Outline platelets.
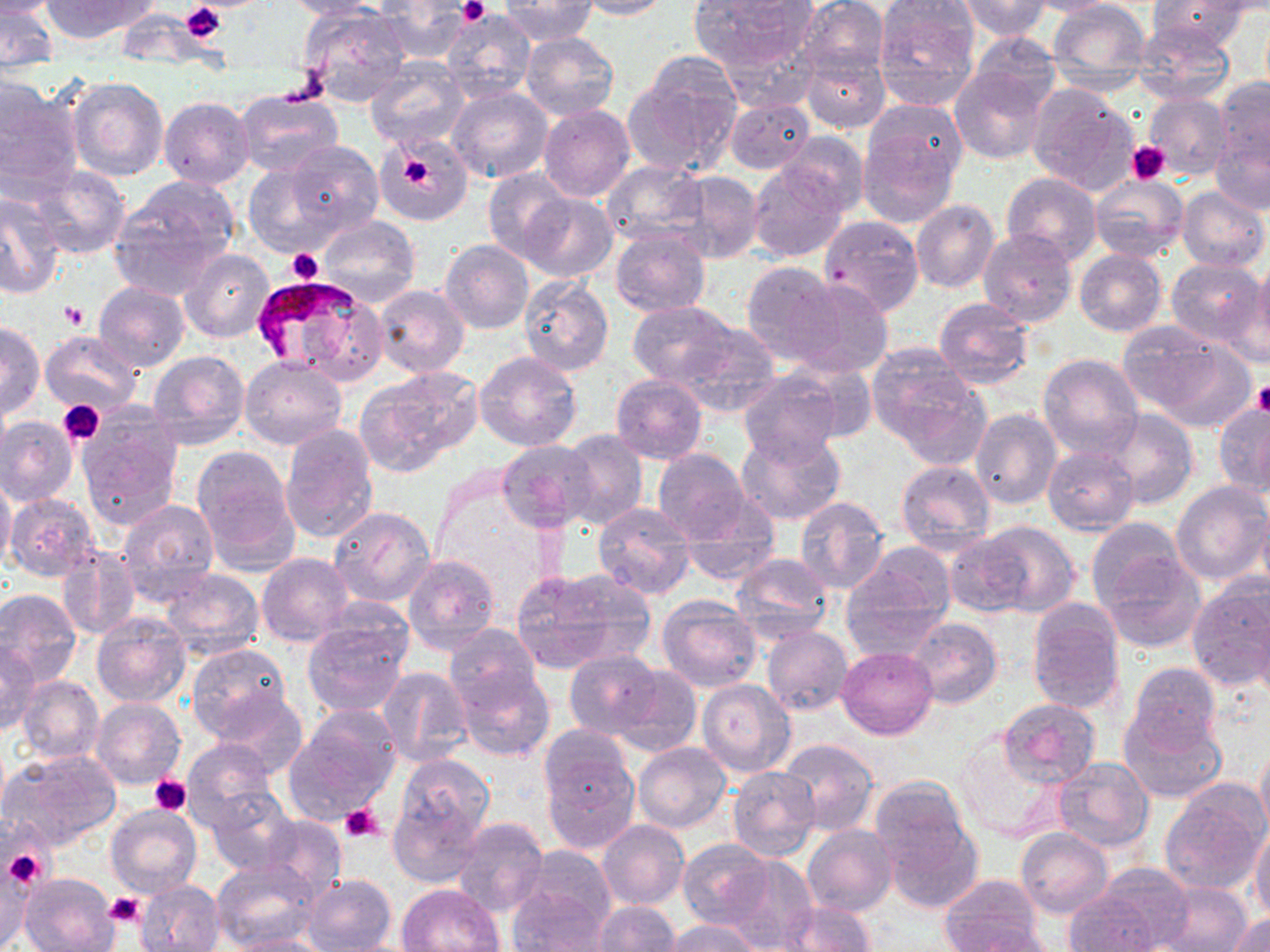

Approximate bounding boxes as named x1/y1/x2/y2 corners in pixels.
Platelets: (x1=459, y1=0, x2=488, y2=24), (x1=181, y1=1, x2=227, y2=42), (x1=279, y1=56, x2=329, y2=107), (x1=1126, y1=141, x2=1172, y2=184), (x1=402, y1=158, x2=435, y2=191), (x1=287, y1=248, x2=323, y2=284), (x1=61, y1=300, x2=87, y2=329), (x1=1253, y1=381, x2=1270, y2=415), (x1=58, y1=400, x2=105, y2=445), (x1=149, y1=775, x2=191, y2=816), (x1=337, y1=803, x2=385, y2=843), (x1=3, y1=846, x2=49, y2=888), (x1=106, y1=892, x2=143, y2=926).

Uninfected red blood cell locations: (x1=1, y1=0, x2=55, y2=18), (x1=41, y1=0, x2=151, y2=41), (x1=282, y1=0, x2=382, y2=19), (x1=575, y1=0, x2=673, y2=20), (x1=691, y1=0, x2=816, y2=74), (x1=873, y1=0, x2=982, y2=110), (x1=954, y1=0, x2=1053, y2=40), (x1=1014, y1=0, x2=1123, y2=16), (x1=1047, y1=0, x2=1148, y2=92), (x1=499, y1=1, x2=597, y2=45), (x1=795, y1=1, x2=889, y2=81), (x1=1149, y1=1, x2=1251, y2=53), (x1=376, y1=2, x2=472, y2=63), (x1=298, y1=5, x2=410, y2=106), (x1=1, y1=7, x2=58, y2=73), (x1=441, y1=8, x2=535, y2=103), (x1=1132, y1=18, x2=1235, y2=107), (x1=520, y1=32, x2=619, y2=121), (x1=961, y1=34, x2=1064, y2=122), (x1=799, y1=50, x2=891, y2=134), (x1=365, y1=59, x2=469, y2=152), (x1=626, y1=61, x2=741, y2=176), (x1=950, y1=63, x2=1052, y2=164), (x1=68, y1=77, x2=168, y2=183), (x1=1213, y1=78, x2=1270, y2=174), (x1=0, y1=79, x2=82, y2=195), (x1=1026, y1=83, x2=1139, y2=195), (x1=447, y1=86, x2=554, y2=184), (x1=236, y1=89, x2=344, y2=177), (x1=1143, y1=94, x2=1233, y2=180), (x1=160, y1=97, x2=254, y2=189), (x1=723, y1=97, x2=815, y2=174), (x1=864, y1=99, x2=968, y2=190), (x1=539, y1=105, x2=635, y2=203), (x1=859, y1=128, x2=957, y2=228), (x1=1210, y1=129, x2=1270, y2=216), (x1=781, y1=132, x2=870, y2=217), (x1=377, y1=133, x2=473, y2=225), (x1=283, y1=141, x2=385, y2=236), (x1=601, y1=159, x2=708, y2=246), (x1=243, y1=161, x2=345, y2=256), (x1=748, y1=162, x2=848, y2=264), (x1=28, y1=166, x2=130, y2=259), (x1=483, y1=167, x2=574, y2=264), (x1=668, y1=170, x2=762, y2=264), (x1=1002, y1=172, x2=1101, y2=266), (x1=1088, y1=173, x2=1188, y2=264), (x1=112, y1=178, x2=238, y2=295), (x1=1176, y1=186, x2=1269, y2=273), (x1=0, y1=193, x2=66, y2=298), (x1=521, y1=193, x2=617, y2=282), (x1=911, y1=199, x2=1000, y2=294), (x1=319, y1=215, x2=419, y2=308), (x1=819, y1=215, x2=924, y2=315), (x1=978, y1=227, x2=1076, y2=329), (x1=611, y1=229, x2=710, y2=318), (x1=440, y1=240, x2=533, y2=333), (x1=181, y1=248, x2=273, y2=343), (x1=1075, y1=248, x2=1167, y2=336), (x1=1251, y1=253, x2=1270, y2=361), (x1=1077, y1=255, x2=1259, y2=341), (x1=1166, y1=259, x2=1265, y2=349), (x1=740, y1=261, x2=839, y2=365), (x1=518, y1=274, x2=614, y2=376), (x1=787, y1=278, x2=894, y2=377), (x1=94, y1=282, x2=189, y2=372), (x1=374, y1=284, x2=469, y2=377), (x1=933, y1=297, x2=1034, y2=390), (x1=629, y1=301, x2=739, y2=386), (x1=1, y1=322, x2=43, y2=419), (x1=676, y1=323, x2=780, y2=416), (x1=1124, y1=324, x2=1251, y2=427), (x1=40, y1=329, x2=142, y2=416), (x1=871, y1=349, x2=990, y2=465), (x1=149, y1=351, x2=249, y2=450), (x1=475, y1=351, x2=582, y2=452), (x1=1037, y1=353, x2=1143, y2=458), (x1=240, y1=355, x2=348, y2=449), (x1=357, y1=366, x2=483, y2=475), (x1=738, y1=372, x2=844, y2=465), (x1=612, y1=375, x2=707, y2=463), (x1=103, y1=384, x2=213, y2=507), (x1=1213, y1=401, x2=1270, y2=496), (x1=77, y1=408, x2=184, y2=530), (x1=969, y1=408, x2=1061, y2=509), (x1=1100, y1=408, x2=1198, y2=510), (x1=0, y1=417, x2=78, y2=506), (x1=278, y1=424, x2=378, y2=544), (x1=737, y1=428, x2=846, y2=526), (x1=560, y1=430, x2=648, y2=531), (x1=496, y1=438, x2=598, y2=531), (x1=190, y1=444, x2=300, y2=571), (x1=1041, y1=444, x2=1140, y2=535), (x1=652, y1=449, x2=751, y2=544), (x1=895, y1=457, x2=996, y2=552), (x1=0, y1=474, x2=15, y2=571), (x1=1170, y1=481, x2=1270, y2=585), (x1=5, y1=494, x2=100, y2=581), (x1=794, y1=496, x2=892, y2=595), (x1=117, y1=498, x2=219, y2=601), (x1=679, y1=498, x2=780, y2=585), (x1=1257, y1=501, x2=1270, y2=601), (x1=592, y1=503, x2=695, y2=599), (x1=329, y1=506, x2=434, y2=607), (x1=1085, y1=517, x2=1189, y2=612), (x1=966, y1=519, x2=1082, y2=616), (x1=943, y1=534, x2=1036, y2=619), (x1=57, y1=545, x2=139, y2=640), (x1=1096, y1=548, x2=1206, y2=651), (x1=730, y1=551, x2=835, y2=644), (x1=257, y1=553, x2=354, y2=646), (x1=403, y1=555, x2=499, y2=657), (x1=839, y1=556, x2=952, y2=656), (x1=161, y1=568, x2=264, y2=658), (x1=509, y1=569, x2=643, y2=674), (x1=1187, y1=579, x2=1269, y2=692), (x1=0, y1=589, x2=83, y2=686), (x1=656, y1=596, x2=760, y2=691), (x1=1026, y1=599, x2=1125, y2=713), (x1=90, y1=610, x2=191, y2=707), (x1=302, y1=617, x2=409, y2=718), (x1=907, y1=617, x2=1002, y2=709), (x1=443, y1=623, x2=540, y2=712), (x1=762, y1=626, x2=854, y2=715), (x1=0, y1=639, x2=40, y2=734), (x1=186, y1=643, x2=293, y2=743), (x1=835, y1=647, x2=937, y2=741), (x1=565, y1=652, x2=665, y2=737), (x1=1126, y1=661, x2=1222, y2=757), (x1=452, y1=664, x2=554, y2=762), (x1=612, y1=665, x2=699, y2=754), (x1=378, y1=667, x2=473, y2=767), (x1=16, y1=675, x2=103, y2=765), (x1=697, y1=679, x2=794, y2=777), (x1=209, y1=690, x2=309, y2=779), (x1=91, y1=697, x2=184, y2=788), (x1=998, y1=698, x2=1101, y2=787), (x1=1118, y1=705, x2=1227, y2=805), (x1=284, y1=709, x2=403, y2=822), (x1=539, y1=723, x2=632, y2=810), (x1=953, y1=736, x2=1064, y2=844), (x1=182, y1=737, x2=279, y2=832), (x1=778, y1=737, x2=879, y2=836), (x1=633, y1=742, x2=731, y2=833), (x1=1255, y1=742, x2=1270, y2=846), (x1=4, y1=750, x2=121, y2=851), (x1=543, y1=752, x2=638, y2=853), (x1=391, y1=753, x2=494, y2=875), (x1=1052, y1=755, x2=1154, y2=852), (x1=728, y1=765, x2=820, y2=861), (x1=1158, y1=779, x2=1268, y2=895), (x1=869, y1=780, x2=982, y2=911), (x1=205, y1=788, x2=300, y2=876), (x1=106, y1=804, x2=201, y2=899), (x1=259, y1=816, x2=346, y2=899), (x1=450, y1=817, x2=548, y2=917), (x1=597, y1=819, x2=688, y2=909), (x1=1250, y1=819, x2=1270, y2=922), (x1=801, y1=823, x2=897, y2=917), (x1=1016, y1=828, x2=1114, y2=918), (x1=677, y1=839, x2=774, y2=932), (x1=712, y1=856, x2=817, y2=950), (x1=0, y1=858, x2=37, y2=949), (x1=212, y1=859, x2=320, y2=951), (x1=1078, y1=864, x2=1195, y2=949), (x1=20, y1=872, x2=119, y2=952), (x1=301, y1=874, x2=397, y2=952), (x1=938, y1=874, x2=1045, y2=950), (x1=136, y1=879, x2=226, y2=952), (x1=395, y1=881, x2=506, y2=952), (x1=1154, y1=881, x2=1253, y2=952), (x1=509, y1=883, x2=611, y2=952), (x1=1065, y1=895, x2=1161, y2=951), (x1=773, y1=900, x2=877, y2=951), (x1=592, y1=901, x2=682, y2=951), (x1=1228, y1=913, x2=1270, y2=951), (x1=664, y1=919, x2=761, y2=952), (x1=955, y1=925, x2=1060, y2=952), (x1=221, y1=934, x2=331, y2=952). Plasmodium falciparum-infected red blood cell locations: (x1=250, y1=273, x2=363, y2=363). Slide-level diagnosis: Plasmodium falciparum. Image is 1270×952 pixels. Captured at 1000x magnification. Thin blood smear. Optical microscopy. May-Grünwald-Giemsa stain. Single field of view.